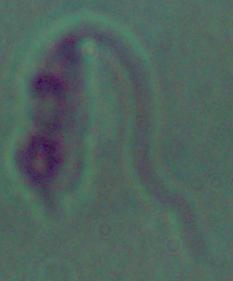
Summary:
  - Identification: Leishmania
  - Modality: photomicrograph
  - Magnification: 1000x